Mark where platelets are.
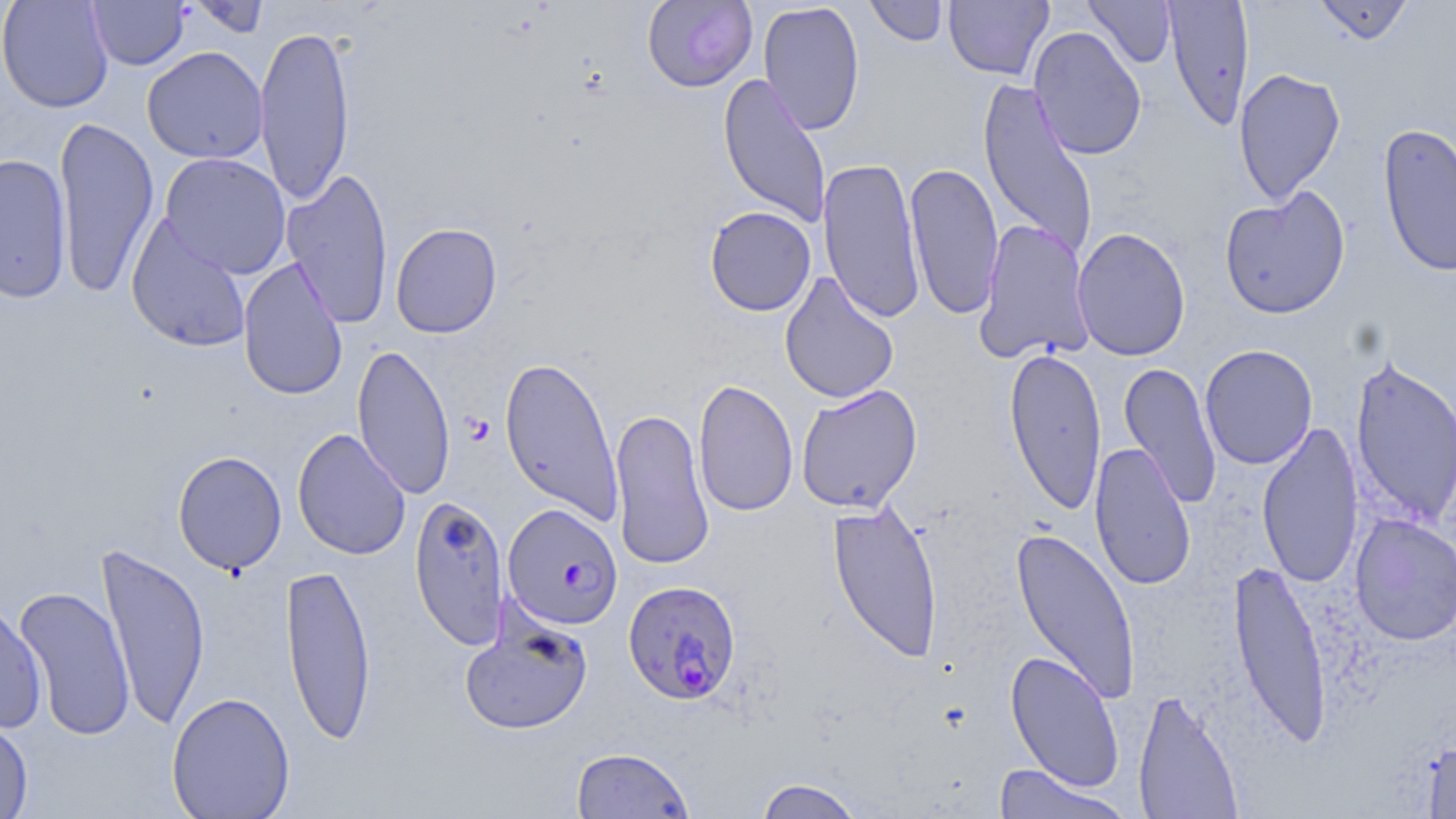

Approximate bounding boxes as named x1/y1/x2/y2 corners in pixels.
Platelets: (x1=461, y1=413, x2=495, y2=446).

slide-level diagnosis = Plasmodium falciparum
modality = optical microscopy
field of view = one of a larger specimen
preparation = thin blood film
uninfected red blood cell locations = approximate bounding boxes as named x1/y1/x2/y2 corners in pixels: (x1=0, y1=0, x2=113, y2=112), (x1=87, y1=0, x2=189, y2=70), (x1=186, y1=0, x2=271, y2=38), (x1=642, y1=0, x2=758, y2=92), (x1=864, y1=0, x2=950, y2=47), (x1=943, y1=0, x2=1053, y2=81), (x1=1083, y1=0, x2=1177, y2=68), (x1=1163, y1=0, x2=1254, y2=132), (x1=1312, y1=0, x2=1414, y2=45), (x1=758, y1=1, x2=865, y2=136), (x1=254, y1=22, x2=355, y2=207), (x1=1028, y1=26, x2=1147, y2=160), (x1=142, y1=46, x2=268, y2=164), (x1=1233, y1=67, x2=1346, y2=205), (x1=717, y1=73, x2=832, y2=228), (x1=978, y1=77, x2=1098, y2=260), (x1=53, y1=114, x2=159, y2=299), (x1=1377, y1=122, x2=1456, y2=278), (x1=0, y1=153, x2=71, y2=304), (x1=159, y1=153, x2=291, y2=279), (x1=817, y1=157, x2=926, y2=324), (x1=905, y1=160, x2=1004, y2=321), (x1=281, y1=167, x2=394, y2=329), (x1=1219, y1=188, x2=1351, y2=319), (x1=704, y1=206, x2=816, y2=316), (x1=126, y1=216, x2=253, y2=353), (x1=975, y1=219, x2=1094, y2=363), (x1=390, y1=222, x2=502, y2=339), (x1=1072, y1=227, x2=1191, y2=361), (x1=238, y1=257, x2=348, y2=401), (x1=780, y1=272, x2=899, y2=404), (x1=1200, y1=343, x2=1318, y2=470), (x1=352, y1=344, x2=456, y2=500), (x1=1003, y1=346, x2=1107, y2=517), (x1=1350, y1=353, x2=1456, y2=529), (x1=498, y1=355, x2=625, y2=525), (x1=1119, y1=361, x2=1223, y2=510), (x1=693, y1=377, x2=798, y2=518), (x1=795, y1=384, x2=922, y2=513), (x1=609, y1=406, x2=715, y2=571), (x1=1256, y1=420, x2=1363, y2=589), (x1=292, y1=427, x2=412, y2=561), (x1=1090, y1=441, x2=1196, y2=591), (x1=173, y1=450, x2=287, y2=575), (x1=410, y1=494, x2=510, y2=650), (x1=827, y1=500, x2=944, y2=664), (x1=1350, y1=513, x2=1456, y2=646), (x1=1009, y1=526, x2=1141, y2=705), (x1=96, y1=540, x2=210, y2=731), (x1=1229, y1=555, x2=1333, y2=750), (x1=281, y1=560, x2=377, y2=745), (x1=14, y1=584, x2=136, y2=741), (x1=0, y1=601, x2=47, y2=734), (x1=459, y1=606, x2=594, y2=735), (x1=1005, y1=650, x2=1125, y2=792), (x1=1132, y1=688, x2=1243, y2=818), (x1=167, y1=692, x2=296, y2=818), (x1=0, y1=716, x2=34, y2=819), (x1=1422, y1=737, x2=1456, y2=819), (x1=571, y1=746, x2=694, y2=819), (x1=991, y1=764, x2=1132, y2=818), (x1=753, y1=777, x2=867, y2=819)
Plasmodium falciparum-infected red blood cell locations = approximate bounding boxes as named x1/y1/x2/y2 corners in pixels: (x1=502, y1=503, x2=623, y2=630), (x1=623, y1=580, x2=742, y2=705)
magnification = 1000x
image size = 1456×819 pixels
stain = May-Grünwald-Giemsa